Name the parasite shown.
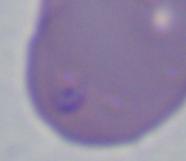

This is Babesia.

{
  "modality": "micrograph",
  "magnification": "1000x"
}